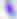 Micrograph. Toxoplasma gondii is seen. 400x magnification.